Name the blood parasite species.
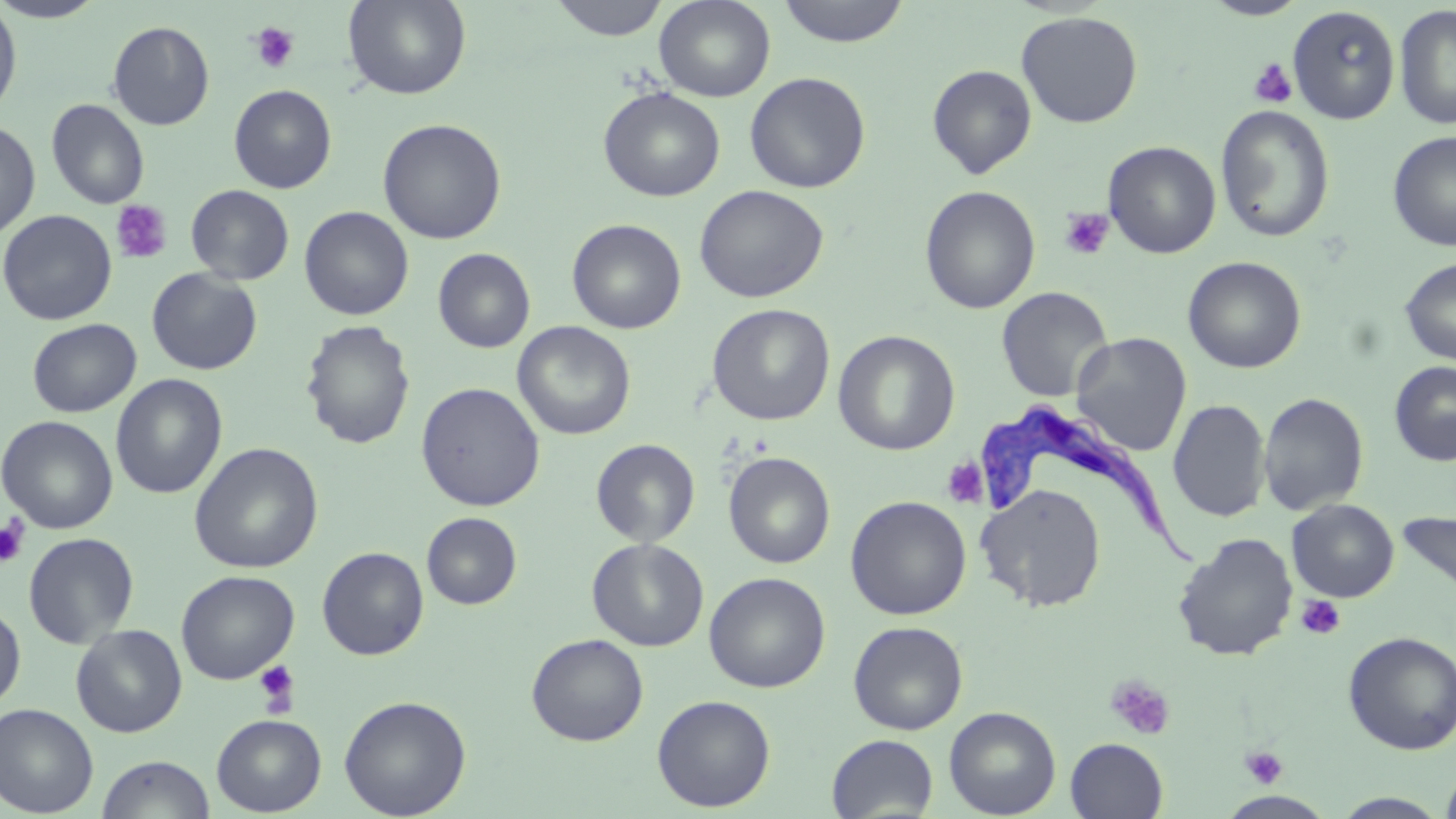
Trypanosoma brucei.

Approximate bounding boxes as (x1,y1)-(x2,y2) corner pairs in pixels. Platelet locations: (249,21)-(300,74), (1248,58)-(1297,108), (110,200)-(173,264), (1058,208)-(1114,261), (941,457)-(988,508), (0,516)-(30,566), (1295,595)-(1345,640), (253,659)-(300,714), (1105,675)-(1175,740), (1240,744)-(1288,789). Trypanosoma brucei locations: (972,401)-(1204,572). Uninfected red blood cell locations: (0,0)-(108,22), (342,0)-(471,100), (550,0)-(668,41), (654,0)-(776,102), (776,0)-(912,48), (1202,0)-(1309,20), (0,2)-(22,119), (1288,5)-(1401,124), (1394,5)-(1456,130), (1015,11)-(1143,128), (107,21)-(215,130), (927,64)-(1037,179), (744,71)-(871,194), (228,84)-(337,193), (598,86)-(725,202), (46,99)-(150,210), (1215,105)-(1335,242), (377,118)-(507,245), (0,121)-(41,240), (1387,130)-(1456,251), (1103,140)-(1221,258), (185,184)-(295,285), (694,184)-(829,303), (919,185)-(1040,314), (299,206)-(414,321), (0,209)-(117,326), (567,218)-(686,334), (433,248)-(535,353), (1182,256)-(1306,374), (1399,258)-(1456,365), (146,268)-(262,375), (996,286)-(1114,402), (707,303)-(835,426), (27,318)-(141,418), (300,320)-(417,451), (512,321)-(636,440), (833,330)-(960,456), (1071,332)-(1192,456), (1389,361)-(1456,466), (111,374)-(228,499), (416,382)-(545,511), (1258,392)-(1369,516), (1168,398)-(1270,523), (1,415)-(118,534), (590,438)-(700,547), (189,442)-(324,574), (723,451)-(836,569), (975,483)-(1107,612), (845,495)-(971,620), (1287,498)-(1399,602), (1397,510)-(1456,601), (421,512)-(522,610), (23,532)-(139,649), (1172,532)-(1298,661), (587,538)-(709,651), (317,546)-(429,660), (175,570)-(299,684), (704,572)-(831,692), (0,604)-(26,711), (848,621)-(968,735), (71,623)-(187,737), (1343,631)-(1456,755), (526,633)-(649,746), (652,694)-(776,812), (338,695)-(471,818), (0,702)-(99,816), (943,706)-(1061,818), (211,714)-(326,816), (826,734)-(938,817), (1065,737)-(1168,818), (97,754)-(215,818), (1440,764)-(1456,819), (1330,792)-(1452,818). Light microscopy. May-Grünwald-Giemsa stain. Thin blood film. One field of a larger specimen. Image is 1456×819 pixels. Captured at 1000x magnification.